Locate every Plasmodium ovale-infected red blood cell.
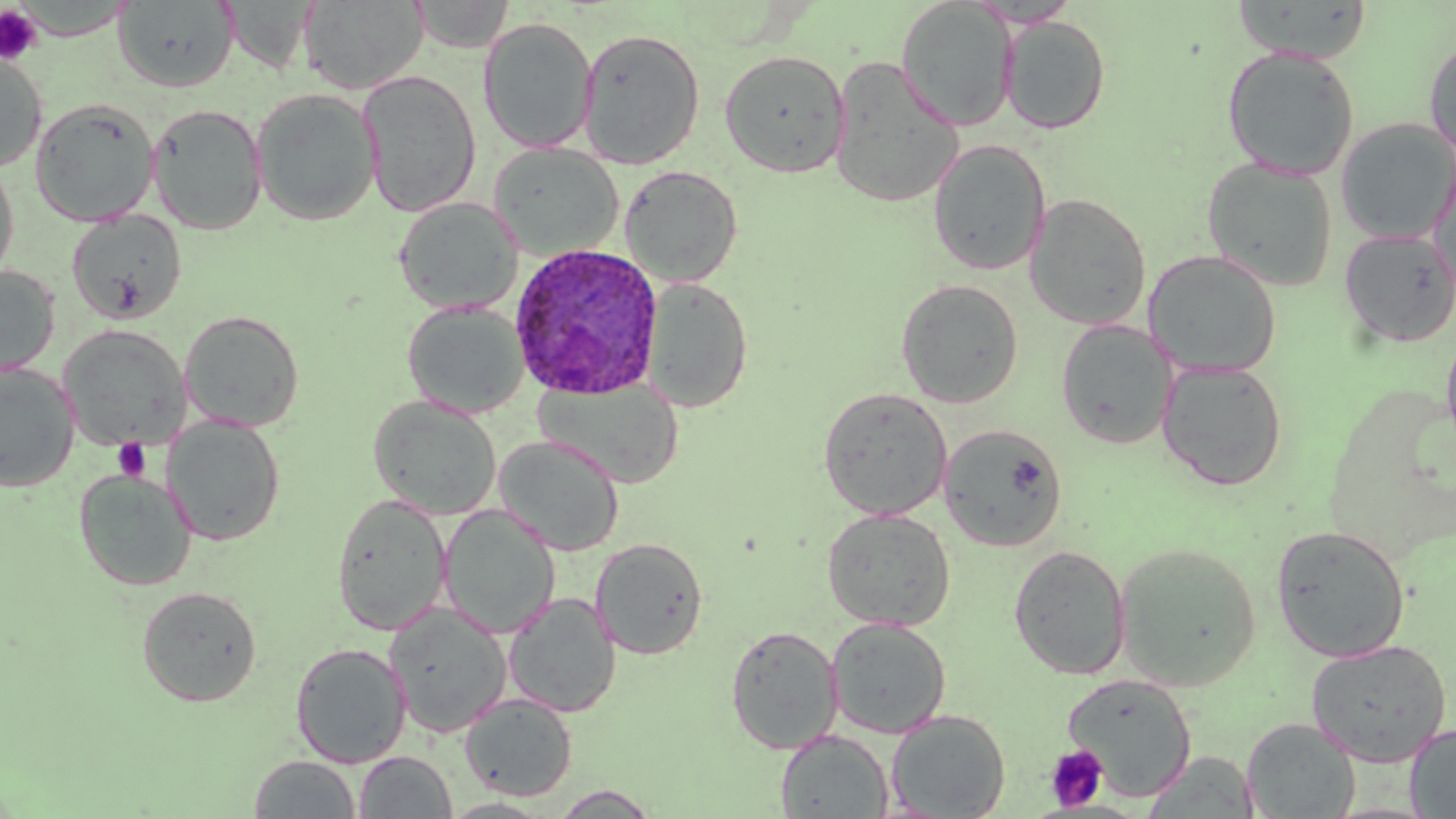
Approximate bounding boxes as (x1,y1)-(x2,y2) corner pairs in pixels.
Plasmodium ovale-infected red blood cells: (508,242)-(664,401).

slide-level diagnosis = Plasmodium ovale
field of view = single
image size = 1456×819 pixels
uninfected red blood cell locations = approximate bounding boxes as (x1,y1)-(x2,y2) corner pairs in pixels: (113,0)-(240,92), (409,0)-(514,53), (896,0)-(1017,130), (1232,0)-(1372,63), (299,1)-(428,94), (1002,16)-(1111,134), (478,17)-(598,154), (577,27)-(705,169), (1424,35)-(1456,160), (1221,45)-(1360,180), (719,49)-(850,177), (0,52)-(47,173), (828,56)-(963,208), (357,69)-(483,217), (250,88)-(382,226), (29,97)-(160,226), (147,103)-(268,235), (1335,117)-(1456,245), (928,139)-(1051,276), (489,142)-(623,260), (0,156)-(20,288), (1201,157)-(1338,292), (490,158)-(746,271), (1429,159)-(1456,304), (620,165)-(743,286), (1024,193)-(1151,330), (393,196)-(523,315), (66,209)-(188,324), (1339,228)-(1456,348), (1144,250)-(1282,377), (0,265)-(60,377), (643,278)-(753,412), (896,279)-(1024,408), (402,300)-(530,418), (179,309)-(305,432), (1056,319)-(1177,449), (1440,324)-(1456,462), (58,325)-(190,451), (1157,360)-(1288,491), (0,362)-(80,493), (535,379)-(684,488), (818,387)-(953,520), (368,396)-(502,520), (161,414)-(286,545), (938,423)-(1068,552), (495,435)-(625,555), (74,469)-(197,590), (330,493)-(452,635), (439,503)-(560,639), (821,508)-(956,631), (1271,525)-(1411,663), (590,537)-(709,659), (1115,542)-(1262,691), (1008,544)-(1132,680), (136,585)-(262,706), (503,591)-(621,718), (385,602)-(512,738), (827,618)-(952,738), (725,624)-(844,754), (1305,639)-(1452,767), (290,641)-(412,768), (1063,674)-(1197,800), (460,693)-(578,801), (886,709)-(1011,818), (1241,717)-(1360,818), (1404,723)-(1456,817), (775,729)-(894,818), (354,751)-(457,818), (1143,751)-(1261,817), (248,755)-(362,818), (549,786)-(661,818)
platelet locations = approximate bounding boxes as (x1,y1)-(x2,y2) corner pairs in pixels: (0,5)-(43,65), (113,437)-(151,481), (1044,745)-(1108,812)
modality = optical microscopy
stain = May-Grünwald-Giemsa
preparation = thin blood film
magnification = 1000x